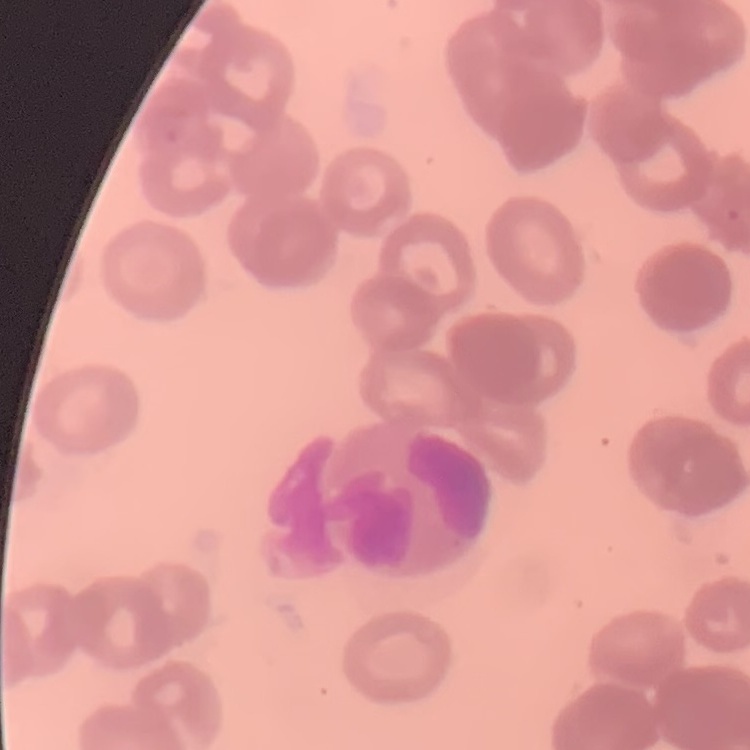

Summary:
  - Red blood cell morphology: rouleaux formation
  - Image type: one tile cut from a larger photomicrograph
  - Preparation: thin blood smear
  - Stain: Field's or Giemsa